State which parasite is depicted.
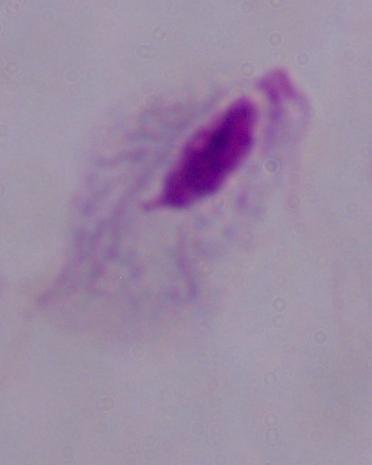

This is a trichomonad.

magnification: 1000x
modality: photomicrograph